Identify the parasite.
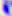

Toxoplasma gondii.

Micrograph. 400x magnification.